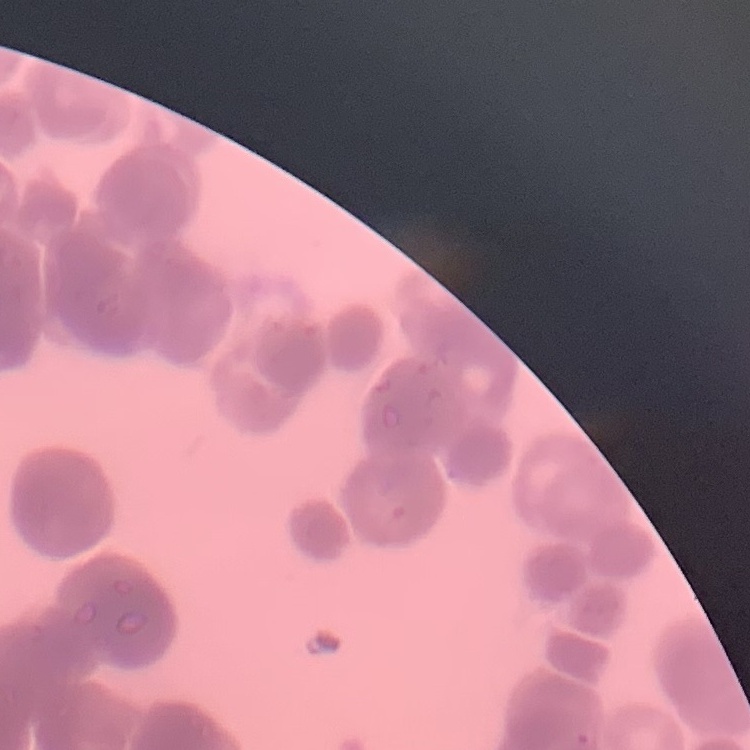

Summary:
  - Red blood cell morphology: rouleaux formation
  - Stain: Field's or Giemsa
  - Preparation: thin blood film
  - Image type: square crop of a larger photomicrograph